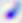
identification: Toxoplasma gondii
magnification: 400x
modality: photomicrograph